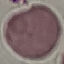
Summary:
  - Malaria status: uninfected
  - Image type: automatically extracted cell patch, resized to 64 × 64 pixels
  - Preparation: thin blood film
  - Capture: smartphone through the microscope eyepiece
  - Stain: Giemsa